Name the parasite shown.
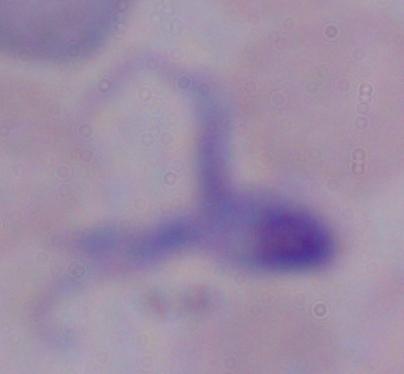
A trypanosome.

magnification = 1000x
modality = micrograph